Report the malaria status of this cell.
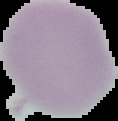

It is uninfected.

The area outside the segmented cell region is set to black. From a thin blood smear. Image is 118×121 pixels.